State which parasite is depicted.
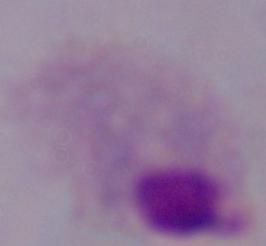
A trichomonad.

Micrograph. 1000x magnification.